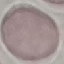
malaria_status: uninfected
stain: Giemsa
image_type: automatically extracted cell patch, resized to 64 × 64 pixels
preparation: thin blood film
capture: smartphone through the microscope eyepiece